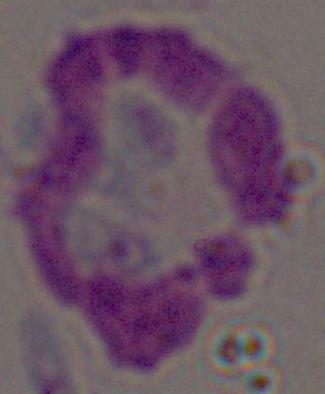

Micrograph. Captured at 1000x magnification. A white blood cell is seen.